Locate Plasmodium parasites and leukocytes.
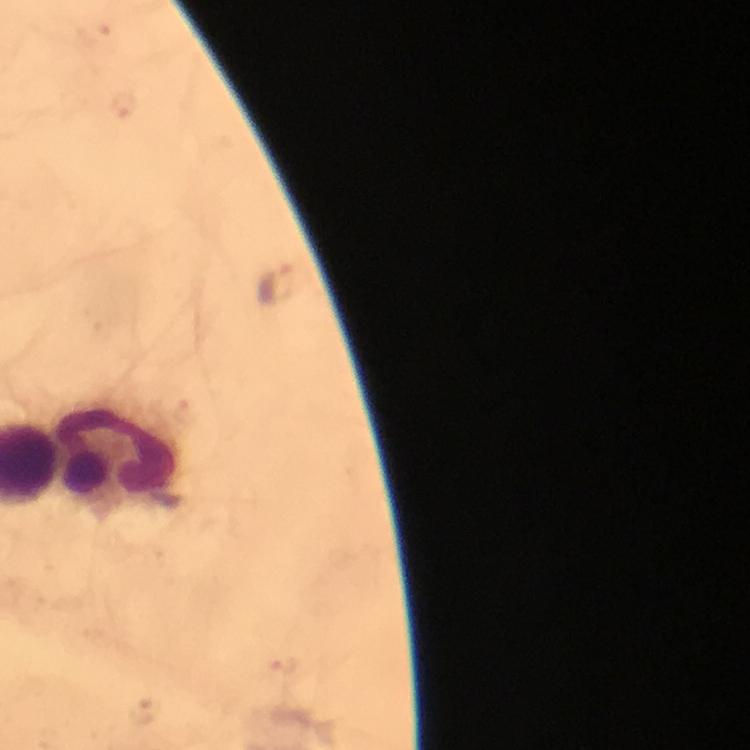

Approximate centers as {x, y} in pixels.
Plasmodium parasites: {127, 105}, {277, 281}, {284, 667}.
Leukocytes: {116, 455}.

Giemsa stain. At 100x magnification. Photographed with a smartphone mounted on the microscope. Image is 750×750 pixels. From a malaria diagnostic workup. Thick blood film. Cropped region of a single field of view. Immersion oil was used.